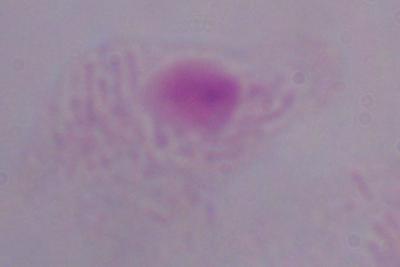 Captured at 1000x magnification. Micrograph. A trichomonad is seen.